State which parasite is depicted.
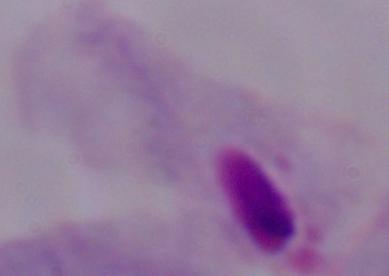

A trichomonad.

Photomicrograph. Captured at 1000x magnification.